Assess this cell for malaria.
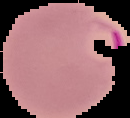

It is parasitized.

From a thin blood film. Segmented cell region on a black background. Image is 130×118 pixels.